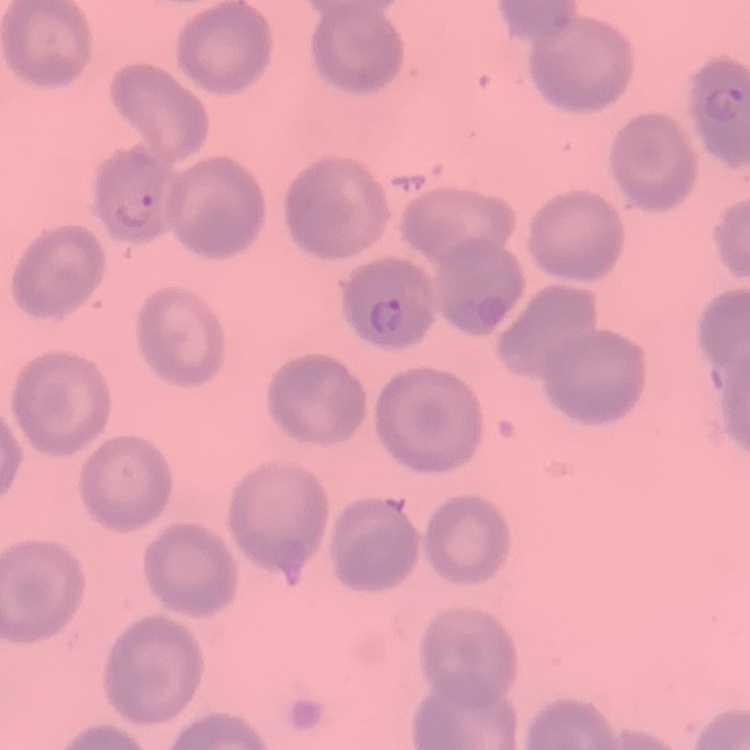 The red blood cells exhibit no rouleaux formation. Thin peripheral smear. Field's or Giemsa stain. One tile cut from a larger photomicrograph.